Locate every Plasmodium vivax-infected red blood cell.
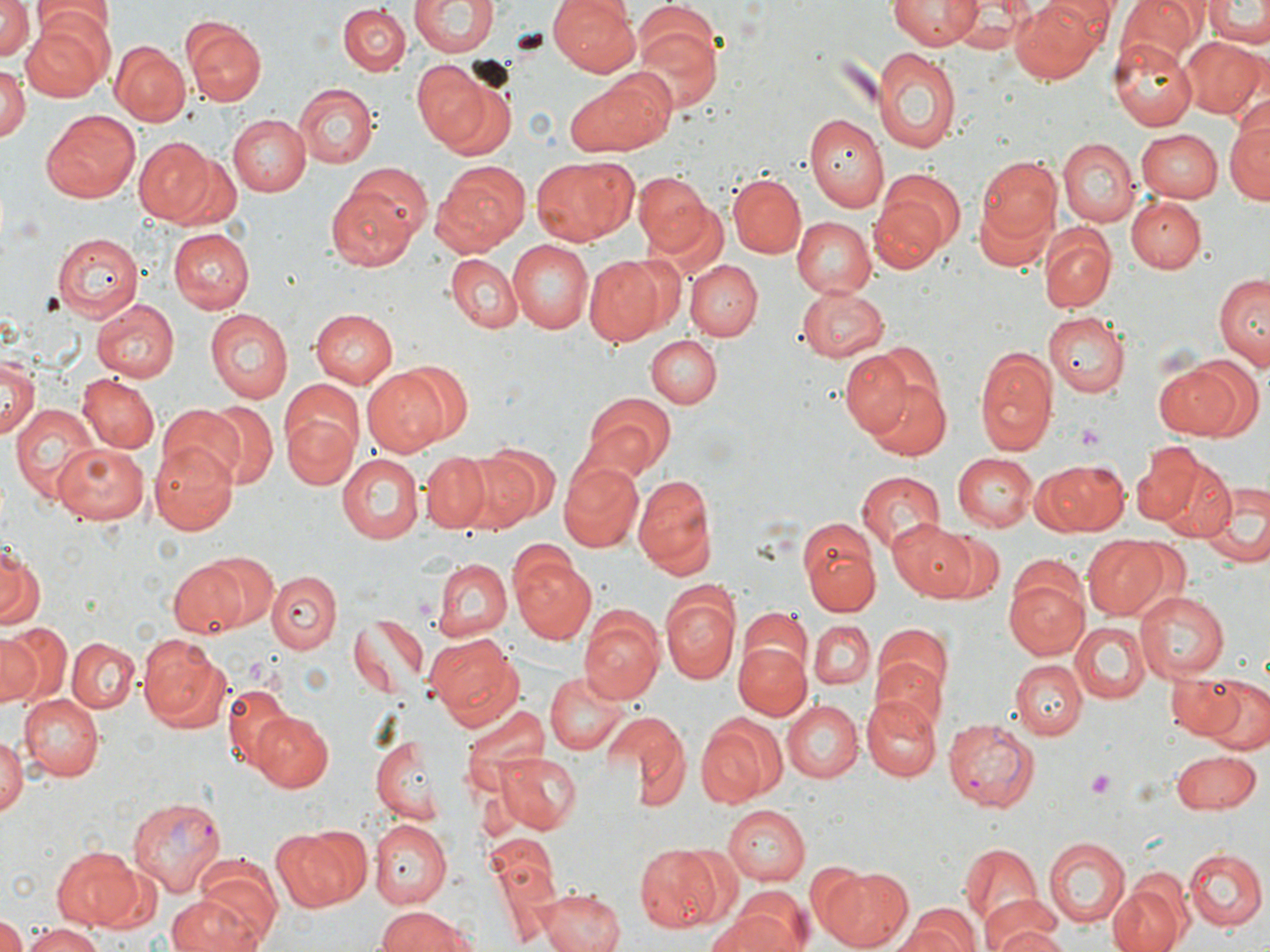
Approximate bounding boxes as named x1/y1/x2/y2 corners in pixels.
Plasmodium vivax-infected red blood cells: (x1=943, y1=718, x2=1039, y2=810), (x1=127, y1=795, x2=226, y2=898).

slide-level diagnosis = Plasmodium vivax
field of view = single
preparation = thin blood film
uninfected red blood cell locations = approximate bounding boxes as named x1/y1/x2/y2 corners in pixels: (x1=409, y1=0, x2=498, y2=59), (x1=549, y1=0, x2=643, y2=75), (x1=886, y1=0, x2=980, y2=50), (x1=1009, y1=0, x2=1106, y2=85), (x1=1117, y1=0, x2=1204, y2=64), (x1=0, y1=1, x2=36, y2=65), (x1=1201, y1=1, x2=1270, y2=47), (x1=339, y1=4, x2=411, y2=75), (x1=32, y1=7, x2=112, y2=55), (x1=21, y1=12, x2=113, y2=99), (x1=630, y1=18, x2=722, y2=114), (x1=185, y1=21, x2=267, y2=105), (x1=1108, y1=36, x2=1199, y2=131), (x1=1181, y1=38, x2=1267, y2=121), (x1=111, y1=40, x2=190, y2=125), (x1=871, y1=44, x2=962, y2=153), (x1=409, y1=60, x2=493, y2=151), (x1=0, y1=65, x2=29, y2=145), (x1=566, y1=72, x2=672, y2=158), (x1=294, y1=85, x2=377, y2=168), (x1=41, y1=109, x2=141, y2=203), (x1=1226, y1=110, x2=1270, y2=206), (x1=804, y1=114, x2=887, y2=213), (x1=227, y1=115, x2=310, y2=196), (x1=1137, y1=129, x2=1223, y2=201), (x1=1060, y1=137, x2=1139, y2=227), (x1=136, y1=139, x2=214, y2=224), (x1=977, y1=155, x2=1065, y2=249), (x1=530, y1=156, x2=634, y2=246), (x1=433, y1=160, x2=529, y2=256), (x1=344, y1=164, x2=434, y2=245), (x1=872, y1=169, x2=963, y2=271), (x1=633, y1=171, x2=715, y2=258), (x1=728, y1=173, x2=806, y2=258), (x1=327, y1=186, x2=422, y2=267), (x1=1126, y1=195, x2=1205, y2=272), (x1=791, y1=218, x2=876, y2=300), (x1=1040, y1=222, x2=1115, y2=313), (x1=53, y1=229, x2=148, y2=320), (x1=168, y1=229, x2=254, y2=313), (x1=507, y1=241, x2=594, y2=334), (x1=61, y1=244, x2=174, y2=376), (x1=445, y1=252, x2=522, y2=334), (x1=583, y1=254, x2=668, y2=345), (x1=685, y1=258, x2=762, y2=339), (x1=1214, y1=275, x2=1269, y2=368), (x1=797, y1=286, x2=888, y2=360), (x1=89, y1=298, x2=178, y2=380), (x1=311, y1=309, x2=397, y2=387), (x1=204, y1=310, x2=293, y2=403), (x1=1044, y1=311, x2=1130, y2=397), (x1=647, y1=335, x2=720, y2=408), (x1=975, y1=347, x2=1057, y2=454), (x1=840, y1=348, x2=920, y2=435), (x1=0, y1=352, x2=41, y2=437), (x1=1154, y1=362, x2=1248, y2=437), (x1=361, y1=367, x2=453, y2=457), (x1=77, y1=373, x2=158, y2=454), (x1=868, y1=378, x2=950, y2=459), (x1=277, y1=380, x2=368, y2=469), (x1=580, y1=396, x2=676, y2=483), (x1=10, y1=401, x2=100, y2=503), (x1=194, y1=403, x2=273, y2=487), (x1=155, y1=405, x2=246, y2=492), (x1=285, y1=413, x2=358, y2=488), (x1=150, y1=440, x2=238, y2=535), (x1=55, y1=443, x2=149, y2=523), (x1=467, y1=446, x2=559, y2=529), (x1=1133, y1=446, x2=1205, y2=525), (x1=951, y1=452, x2=1036, y2=532), (x1=338, y1=453, x2=426, y2=543), (x1=422, y1=453, x2=490, y2=531), (x1=556, y1=455, x2=648, y2=553), (x1=1035, y1=457, x2=1130, y2=536), (x1=1156, y1=458, x2=1238, y2=542), (x1=631, y1=468, x2=718, y2=578), (x1=854, y1=470, x2=944, y2=554), (x1=1200, y1=484, x2=1269, y2=567), (x1=888, y1=518, x2=980, y2=600), (x1=800, y1=522, x2=877, y2=615), (x1=940, y1=529, x2=1005, y2=602), (x1=1082, y1=536, x2=1169, y2=619), (x1=0, y1=545, x2=43, y2=631), (x1=200, y1=550, x2=283, y2=632), (x1=513, y1=554, x2=596, y2=645), (x1=429, y1=557, x2=511, y2=643), (x1=168, y1=559, x2=251, y2=638), (x1=266, y1=571, x2=343, y2=653), (x1=1005, y1=571, x2=1089, y2=660), (x1=662, y1=587, x2=739, y2=685), (x1=1134, y1=590, x2=1230, y2=680), (x1=741, y1=607, x2=811, y2=679), (x1=581, y1=611, x2=665, y2=707), (x1=347, y1=615, x2=428, y2=700), (x1=809, y1=620, x2=875, y2=691), (x1=1069, y1=621, x2=1148, y2=704), (x1=1, y1=625, x2=69, y2=708), (x1=874, y1=630, x2=951, y2=725), (x1=425, y1=633, x2=518, y2=722), (x1=136, y1=635, x2=232, y2=735), (x1=68, y1=637, x2=139, y2=713), (x1=734, y1=641, x2=810, y2=721), (x1=1011, y1=660, x2=1087, y2=739), (x1=546, y1=672, x2=630, y2=755), (x1=1169, y1=674, x2=1241, y2=737), (x1=1205, y1=682, x2=1270, y2=754), (x1=221, y1=685, x2=288, y2=771), (x1=18, y1=693, x2=103, y2=781), (x1=862, y1=694, x2=940, y2=781), (x1=781, y1=699, x2=862, y2=783), (x1=458, y1=701, x2=546, y2=796), (x1=250, y1=712, x2=334, y2=793), (x1=608, y1=714, x2=687, y2=808), (x1=695, y1=715, x2=782, y2=805), (x1=0, y1=732, x2=24, y2=818), (x1=370, y1=736, x2=446, y2=823), (x1=491, y1=749, x2=584, y2=834), (x1=1171, y1=750, x2=1260, y2=817), (x1=722, y1=806, x2=810, y2=884), (x1=369, y1=821, x2=449, y2=909), (x1=275, y1=825, x2=369, y2=911), (x1=485, y1=829, x2=558, y2=897), (x1=1043, y1=838, x2=1130, y2=926), (x1=958, y1=841, x2=1043, y2=933), (x1=51, y1=845, x2=144, y2=929), (x1=634, y1=845, x2=733, y2=931), (x1=1183, y1=847, x2=1265, y2=932), (x1=190, y1=862, x2=283, y2=948), (x1=819, y1=865, x2=914, y2=952), (x1=1108, y1=879, x2=1189, y2=952), (x1=538, y1=889, x2=625, y2=952), (x1=167, y1=893, x2=265, y2=952), (x1=707, y1=900, x2=806, y2=952), (x1=377, y1=905, x2=475, y2=952), (x1=901, y1=905, x2=981, y2=952), (x1=982, y1=906, x2=1068, y2=952), (x1=0, y1=917, x2=25, y2=952), (x1=24, y1=922, x2=102, y2=952)
stain = May-Grünwald-Giemsa
platelet locations = approximate bounding boxes as named x1/y1/x2/y2 corners in pixels: (x1=1075, y1=423, x2=1105, y2=449), (x1=1086, y1=769, x2=1116, y2=799)
magnification = 1000x
modality = light microscopy
image size = 1270×952 pixels